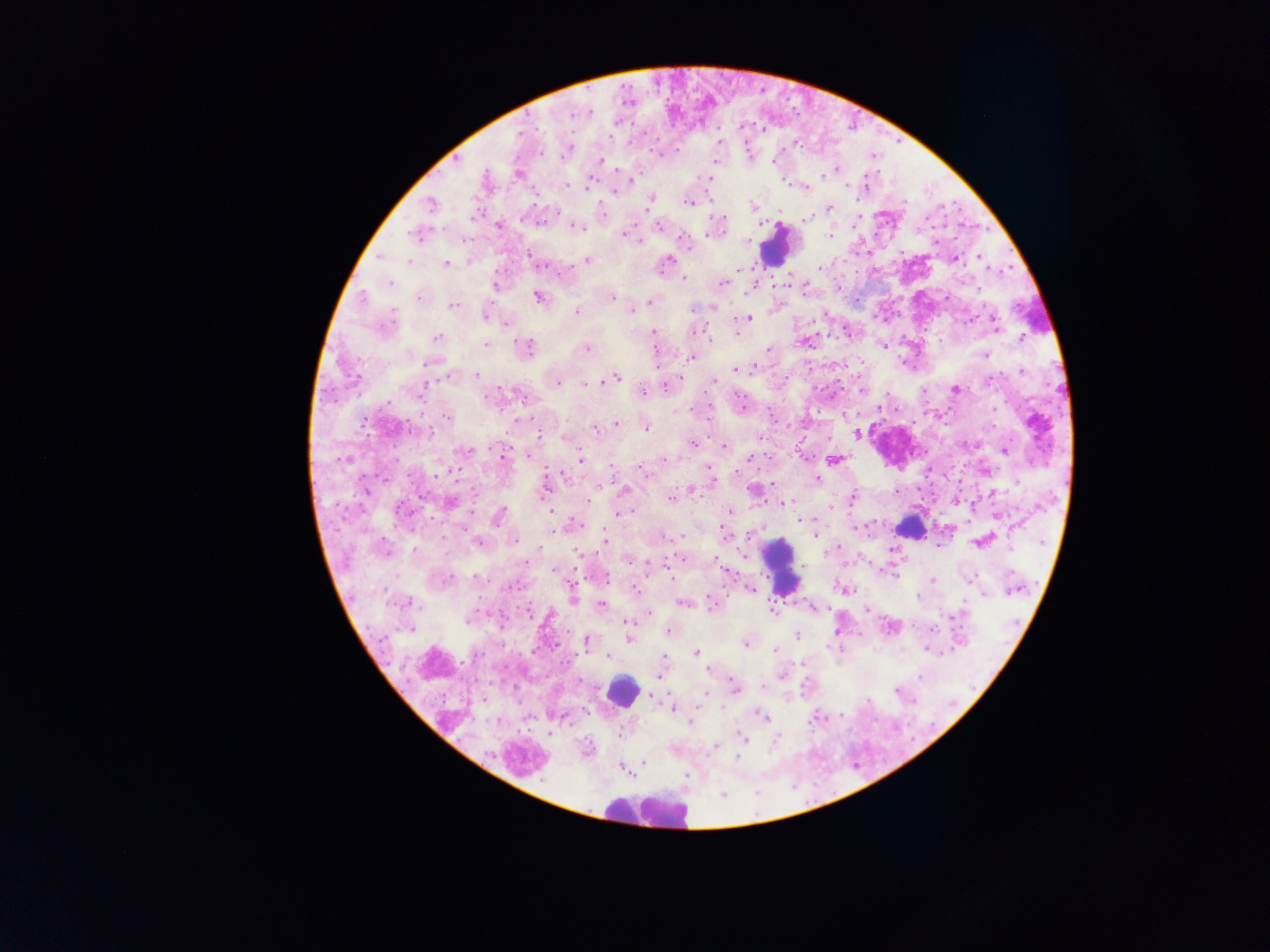
Approximate centers as [x, y] in pixels.
Summary:
  - Leukocyte locations: [776, 246], [1040, 425], [911, 526], [781, 566], [622, 692], [643, 808]
  - Plasmodium parasite locations: [590, 112], [570, 115], [521, 133], [563, 155], [600, 161], [774, 161], [837, 168], [517, 174], [823, 175], [867, 175], [708, 178], [631, 179], [587, 184], [567, 185], [847, 185], [806, 188], [614, 192], [650, 199], [689, 204], [430, 205], [648, 205], [831, 208], [808, 219], [498, 225], [659, 225], [577, 228], [414, 234], [709, 234], [624, 235], [830, 237], [684, 238], [379, 256], [529, 256], [980, 257], [955, 259], [586, 260], [408, 261], [668, 261], [446, 263], [539, 265], [738, 268], [820, 268], [683, 278], [390, 283], [723, 284], [495, 286], [839, 288], [362, 298], [418, 298], [537, 298], [612, 298], [649, 302], [453, 306], [712, 307], [692, 308], [577, 311], [631, 311], [392, 316], [485, 317], [748, 318], [506, 324], [994, 325], [654, 332], [736, 333], [1021, 337], [436, 338], [710, 338], [486, 344], [884, 346], [527, 347], [587, 349], [769, 349], [985, 355], [691, 357], [427, 363], [736, 369], [752, 369], [1022, 371], [476, 375], [616, 377], [990, 380], [599, 381], [713, 381], [557, 383], [586, 384], [425, 385], [665, 387], [955, 390], [861, 391], [643, 392], [739, 397], [386, 402], [878, 408], [995, 409], [446, 417], [516, 420], [617, 423], [363, 424], [646, 427], [596, 429], [430, 433], [857, 434], [539, 436], [564, 437], [760, 438], [692, 444], [724, 446], [464, 450], [1004, 451], [502, 455], [750, 458], [344, 459], [663, 459], [581, 460], [834, 461], [458, 467], [610, 467], [438, 475], [564, 475], [646, 475], [817, 479], [712, 481], [773, 483], [692, 490], [623, 491], [993, 492], [474, 493], [422, 497], [854, 497], [671, 499], [588, 500], [450, 503], [783, 503], [831, 507], [729, 511], [402, 512], [550, 512], [620, 514], [499, 516], [997, 517], [800, 521], [578, 524], [552, 530], [723, 531], [682, 536], [815, 536], [515, 541], [604, 541], [478, 542], [978, 542], [539, 547], [837, 548], [1010, 548], [414, 550], [577, 553], [629, 560], [717, 561], [553, 571], [476, 579], [446, 580], [932, 580], [970, 581], [635, 588], [750, 588], [1014, 591], [918, 597], [573, 598], [405, 603], [683, 604], [600, 605], [713, 606], [771, 610], [649, 613], [954, 615], [467, 620], [627, 623], [411, 629], [932, 629], [669, 632], [796, 635], [630, 637], [588, 642], [745, 644], [774, 650], [696, 653], [476, 656], [608, 657], [665, 657], [709, 668], [781, 675], [919, 676], [735, 687], [763, 687], [897, 691], [704, 695], [651, 696], [673, 709], [762, 715], [690, 723], [619, 735], [744, 738], [716, 746], [643, 763]
  - Preparation: thick blood film
  - Country: Ghana
  - Image size: 1270×952 pixels
  - Field of view: single
  - Capture: mobile-phone photograph through a microscope